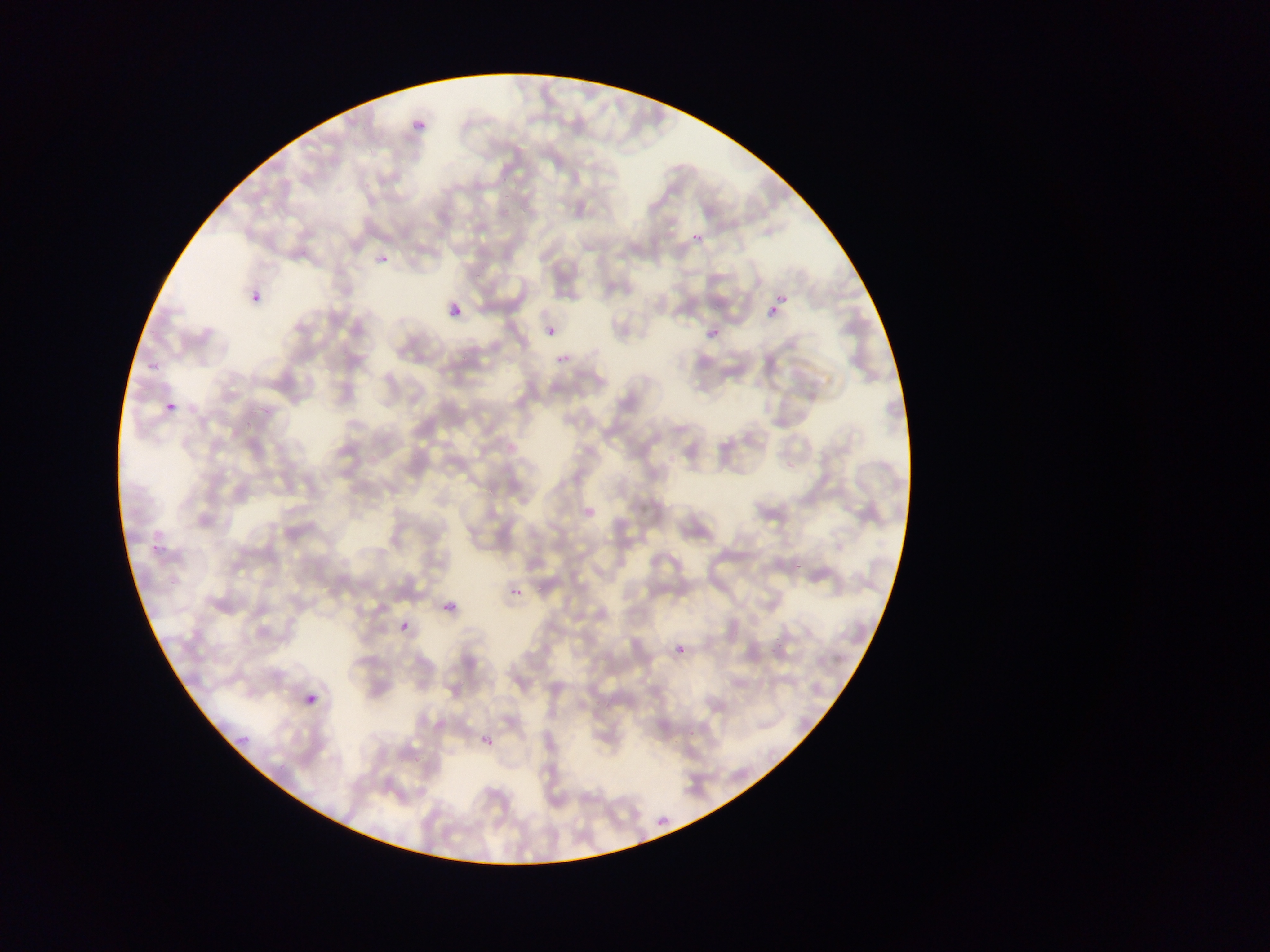

Approximate bounding boxes as [left, top, right, bottom] in pixels.
Summary:
  - Malaria parasite locations: [413, 111, 429, 127], [689, 229, 707, 250], [379, 253, 392, 267], [247, 284, 268, 305], [764, 297, 788, 325], [446, 298, 469, 326], [543, 325, 559, 343], [703, 327, 721, 345], [163, 399, 179, 417], [506, 582, 526, 604], [439, 595, 462, 620], [393, 623, 414, 638], [673, 641, 688, 658], [301, 687, 326, 714], [228, 724, 253, 744], [477, 730, 499, 753], [648, 808, 679, 825]
  - Image size: 1270×952 pixels
  - Country: Ghana
  - Capture: mobile-phone photograph through a microscope
  - Field of view: single
  - Preparation: thin blood film